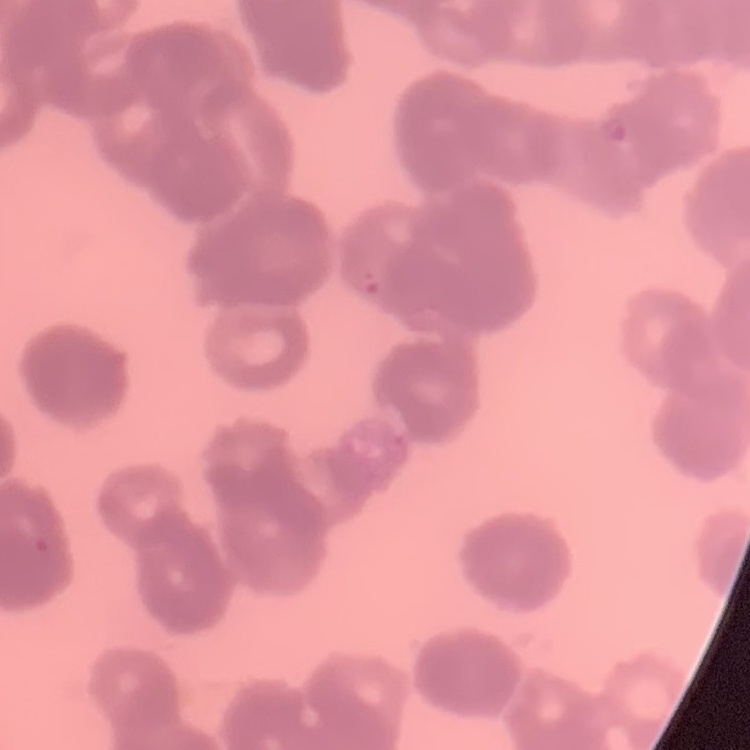

{
  "erythrocyte_morphology": "rouleaux formation",
  "stain": "Field's or Giemsa",
  "preparation": "thin blood smear",
  "image_type": "one tile cut from a larger photomicrograph"
}